Name the blood parasite species.
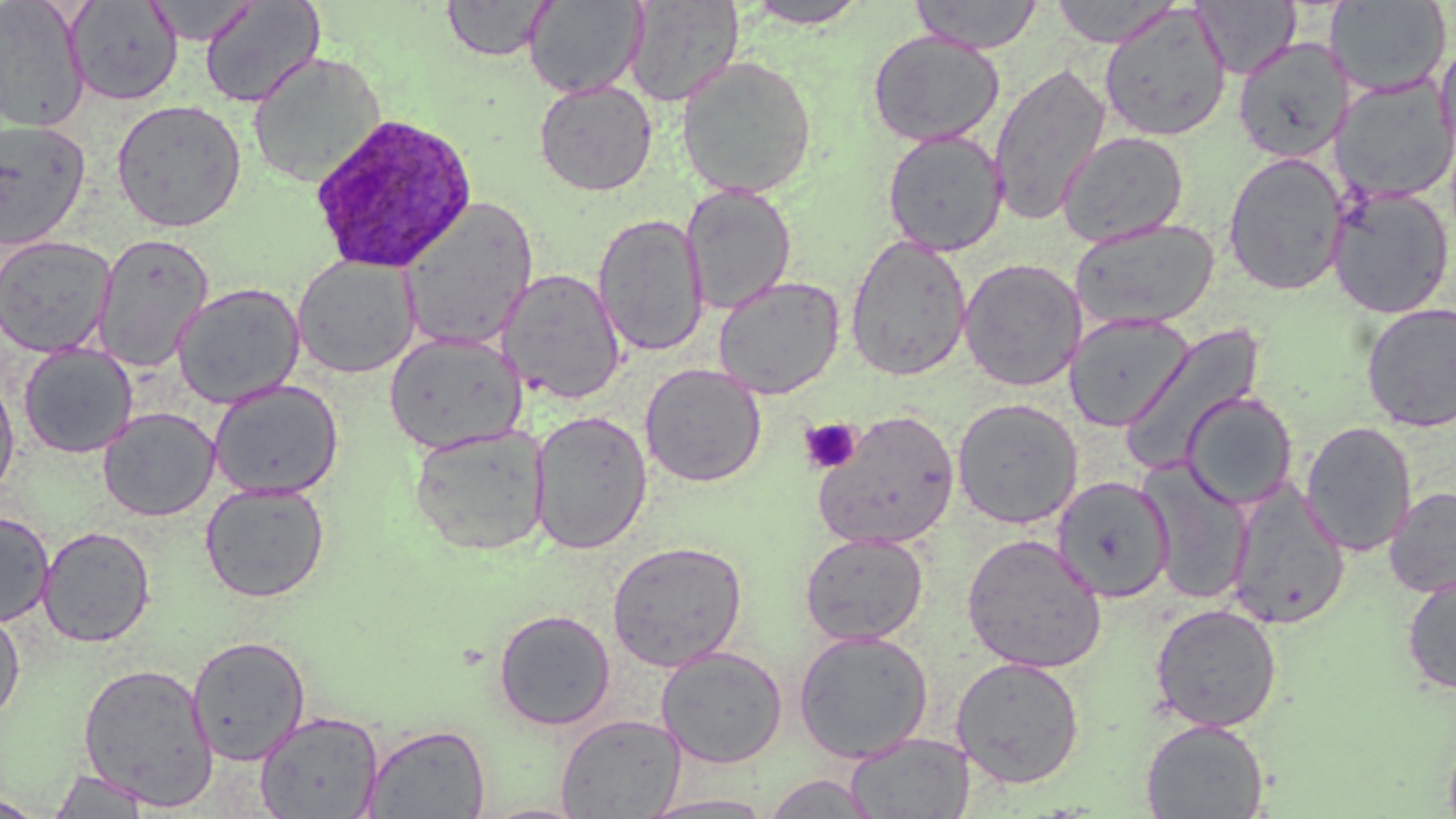
Plasmodium ovale.

{
  "platelet_locations": "approximate bounding boxes as [x1, y1, x2, y2] in pixels: [799, 417, 862, 474]",
  "uninfected_red_blood_cell_locations": "approximate bounding boxes as [x1, y1, x2, y2] in pixels: [0, 0, 90, 133], [623, 0, 744, 107], [909, 0, 1043, 53], [1326, 0, 1452, 97], [65, 1, 183, 106], [143, 1, 258, 46], [198, 1, 325, 109], [441, 1, 554, 61], [524, 1, 647, 99], [744, 1, 870, 28], [1049, 1, 1181, 48], [1193, 1, 1299, 79], [1098, 5, 1232, 142], [868, 31, 1005, 147], [1233, 36, 1353, 163], [1433, 39, 1456, 160], [248, 50, 388, 188], [676, 55, 817, 198], [988, 61, 1112, 226], [1333, 75, 1456, 204], [534, 79, 658, 196], [111, 98, 247, 232], [0, 119, 91, 250], [882, 128, 1008, 256], [1057, 130, 1189, 248], [1223, 151, 1349, 296], [680, 183, 798, 316], [1328, 187, 1454, 319], [397, 196, 540, 351], [592, 213, 709, 357], [1070, 217, 1220, 331], [92, 232, 214, 371], [0, 235, 116, 357], [845, 235, 973, 381], [292, 256, 421, 379], [958, 258, 1086, 391], [497, 268, 627, 405], [713, 275, 844, 399], [172, 282, 306, 409], [1360, 302, 1456, 432], [1064, 313, 1195, 432], [1118, 320, 1269, 472], [384, 331, 527, 455], [18, 343, 138, 458], [640, 363, 766, 487], [0, 374, 19, 500], [208, 379, 344, 500], [1182, 392, 1298, 509], [952, 397, 1083, 529], [98, 407, 220, 522], [813, 409, 960, 550], [529, 410, 652, 555], [1300, 421, 1418, 557], [408, 424, 551, 557], [1139, 461, 1253, 606], [1052, 475, 1175, 604], [200, 482, 330, 602], [1225, 482, 1351, 630], [1384, 486, 1456, 597], [0, 511, 54, 626], [37, 525, 156, 647], [799, 531, 929, 647], [962, 533, 1107, 674], [606, 539, 748, 672], [1401, 571, 1456, 696], [1149, 603, 1283, 732], [0, 606, 25, 723], [493, 608, 616, 731], [793, 629, 934, 763], [187, 635, 311, 765], [655, 645, 789, 768], [950, 656, 1086, 789], [77, 661, 218, 809], [254, 711, 383, 819], [555, 712, 686, 818], [1140, 718, 1269, 818], [363, 722, 491, 818], [846, 732, 975, 817], [47, 769, 155, 817], [761, 773, 883, 818], [636, 793, 777, 818], [0, 795, 48, 817], [476, 802, 592, 819]",
  "magnification": "1000x",
  "modality": "light microscopy",
  "image_size": "1456×819 pixels",
  "preparation": "thin blood film",
  "plasmodium_ovale_infected_red_blood_cell_locations": "approximate bounding boxes as [x1, y1, x2, y2] in pixels: [308, 113, 477, 274]",
  "field_of_view": "single",
  "stain": "May-Grünwald-Giemsa"
}